Name the blood parasite species.
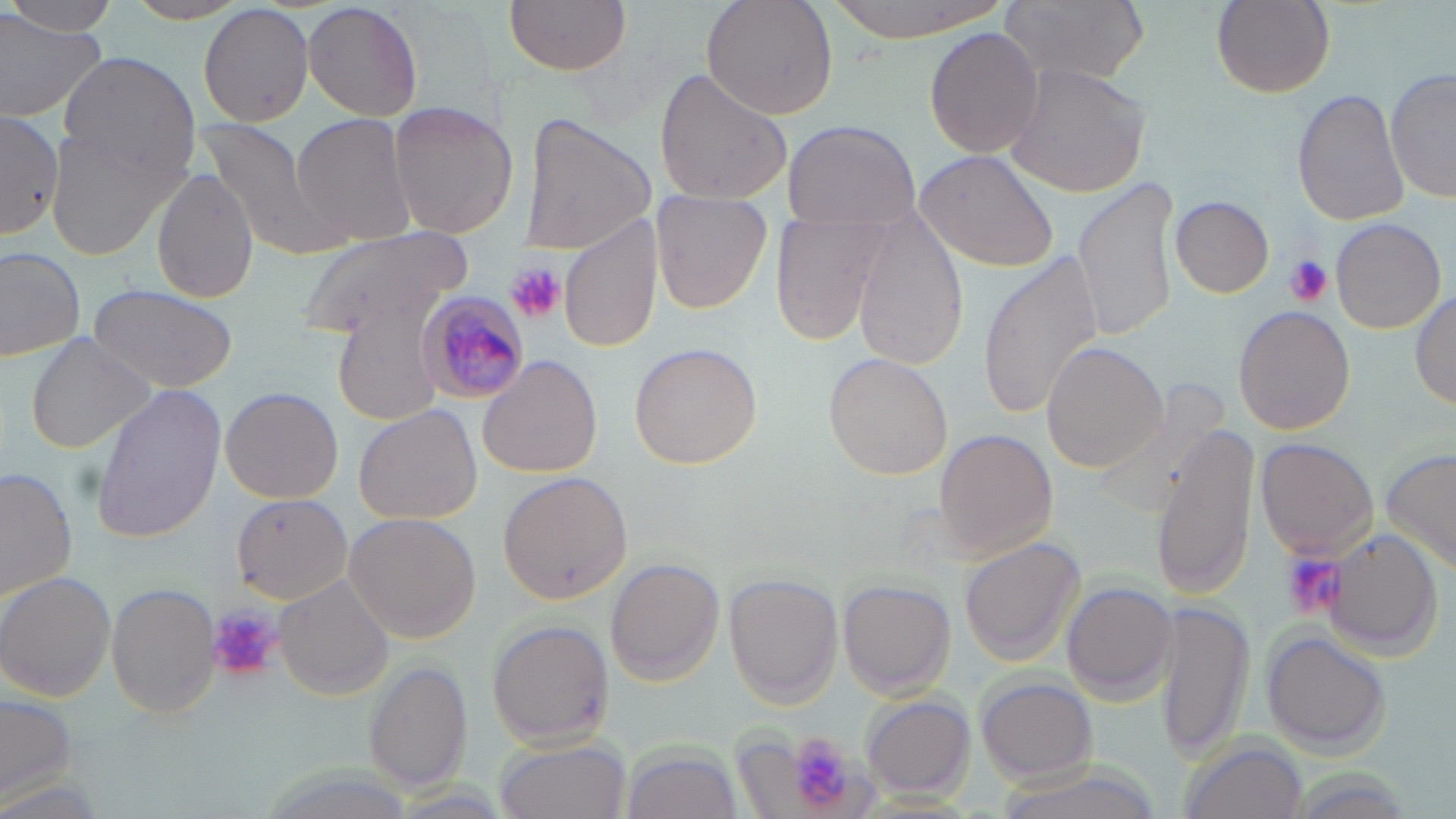
Plasmodium malariae.

Approximate bounding boxes as (x1, y1, x2, y2) in pixels. Plasmodium malariae-infected red blood cell locations: (417, 290, 528, 408). Uninfected red blood cell locations: (5, 0, 126, 39), (303, 0, 423, 121), (504, 0, 632, 76), (700, 0, 840, 118), (817, 0, 1012, 41), (1002, 0, 1147, 86), (1212, 0, 1335, 99), (198, 2, 317, 128), (0, 10, 108, 122), (922, 26, 1044, 160), (59, 51, 199, 178), (1006, 63, 1151, 199), (654, 67, 794, 206), (1386, 70, 1455, 203), (1290, 89, 1410, 226), (388, 100, 520, 240), (1, 110, 61, 240), (289, 113, 417, 246), (519, 114, 655, 255), (194, 117, 330, 251), (44, 118, 187, 260), (780, 118, 921, 229), (918, 149, 1062, 275), (152, 170, 260, 303), (1074, 176, 1180, 341), (652, 192, 775, 315), (1171, 197, 1274, 297), (768, 210, 894, 349), (557, 214, 662, 357), (853, 214, 970, 369), (1331, 217, 1447, 335), (292, 229, 472, 343), (0, 247, 85, 362), (979, 249, 1104, 417), (86, 284, 238, 391), (1412, 285, 1455, 413), (1233, 307, 1355, 435), (24, 332, 157, 455), (629, 342, 763, 470), (1042, 342, 1166, 471), (477, 354, 602, 479), (823, 354, 953, 480), (90, 385, 226, 544), (219, 387, 343, 504), (354, 403, 482, 525), (1153, 423, 1262, 598), (935, 430, 1055, 557), (1255, 437, 1380, 562), (1379, 448, 1456, 576), (2, 467, 78, 602), (496, 471, 632, 605), (231, 494, 355, 606), (344, 512, 482, 644), (1327, 529, 1450, 657), (960, 538, 1085, 666), (604, 558, 724, 685), (1, 573, 118, 699), (725, 575, 842, 706), (275, 576, 394, 699), (839, 580, 954, 697), (1063, 581, 1178, 702), (107, 582, 220, 720), (1153, 599, 1256, 766), (488, 619, 615, 751), (1260, 629, 1391, 760), (365, 659, 470, 793), (975, 677, 1098, 784), (1, 692, 79, 803), (862, 696, 975, 800), (494, 737, 630, 819), (1178, 737, 1310, 819), (624, 742, 737, 818). Platelet locations: (1283, 256, 1332, 307), (504, 261, 564, 324), (1281, 554, 1345, 621), (208, 606, 278, 679), (787, 733, 853, 809). 1000x magnification. Thin blood film. May-Grünwald-Giemsa-stained preparation. One field of a larger specimen. Image is 1456×819 pixels. Light microscopy.